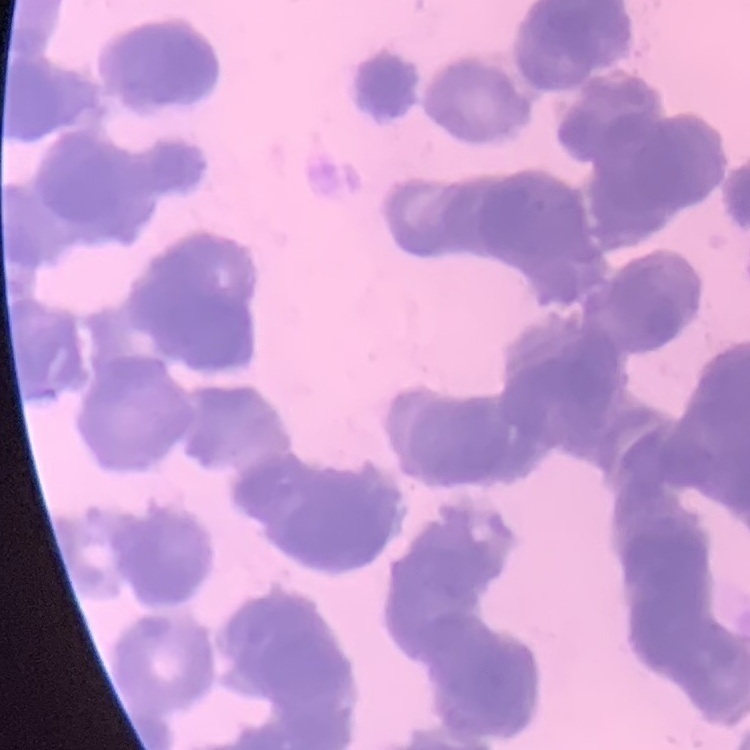
red blood cell morphology = rouleaux formation
preparation = thin blood film
stain = Field's or Giemsa
image type = one tile cut from a larger photomicrograph